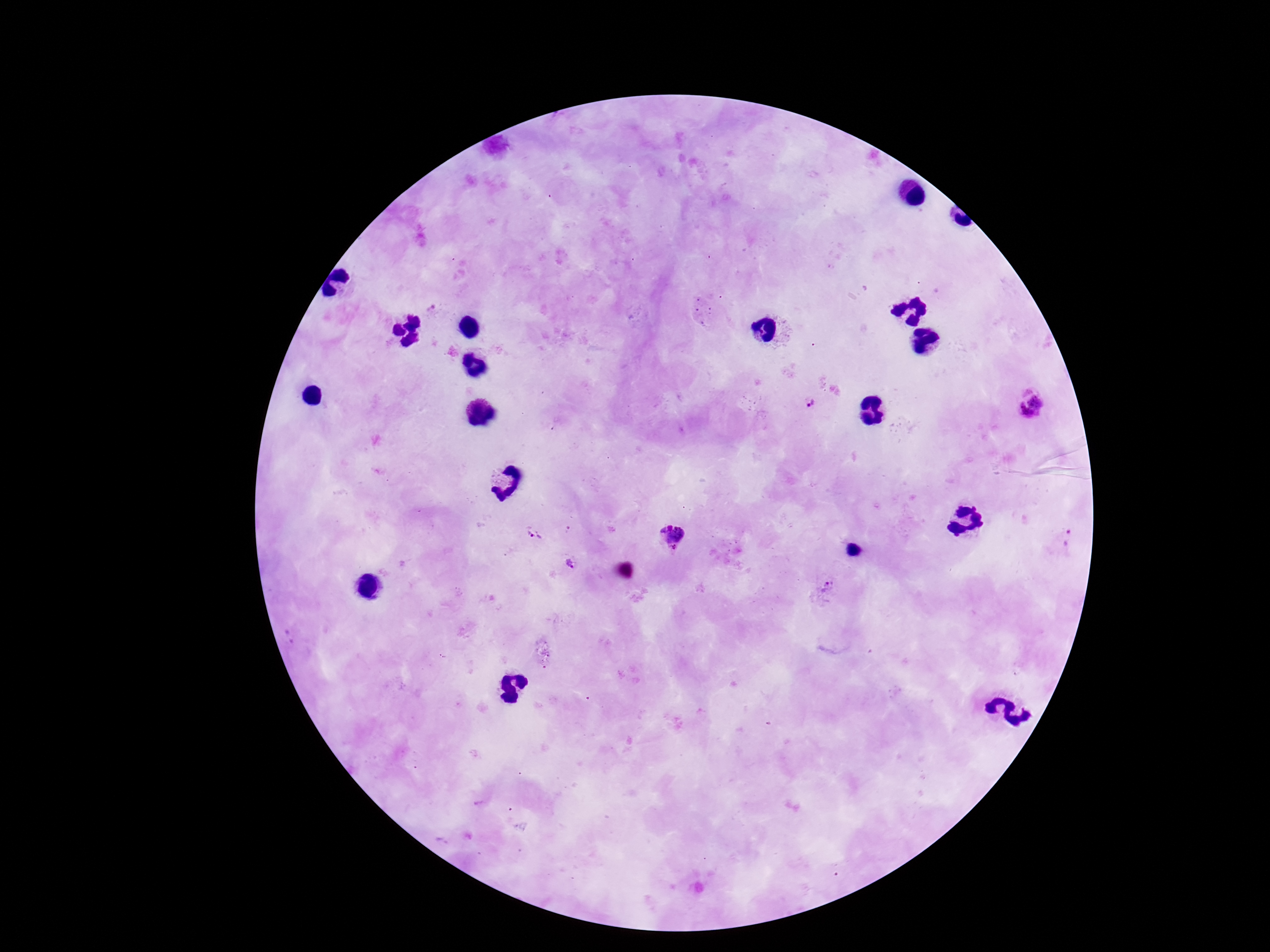
patient malaria status = positive
capture = smartphone camera through the microscope eyepiece
Plasmodium parasite locations = approximate object centers, in pixels from the top-left corner: (x=1032, y=402), (x=809, y=404), (x=530, y=535), (x=672, y=535), (x=1069, y=539), (x=573, y=564), (x=824, y=590)
magnification = 100x
image size = 1270×952 pixels
stain = Giemsa
preparation = thick peripheral-blood smear
field of view = one from this slide